Report the malaria status of this cell.
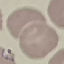

It is parasitized.

Cell patch, automatically extracted from a larger field of view and resized to 64 × 64 pixels. Thin smear of blood. Giemsa-stained preparation. Acquired by smartphone through the microscope eyepiece.